Outline each uninfected red blood cell.
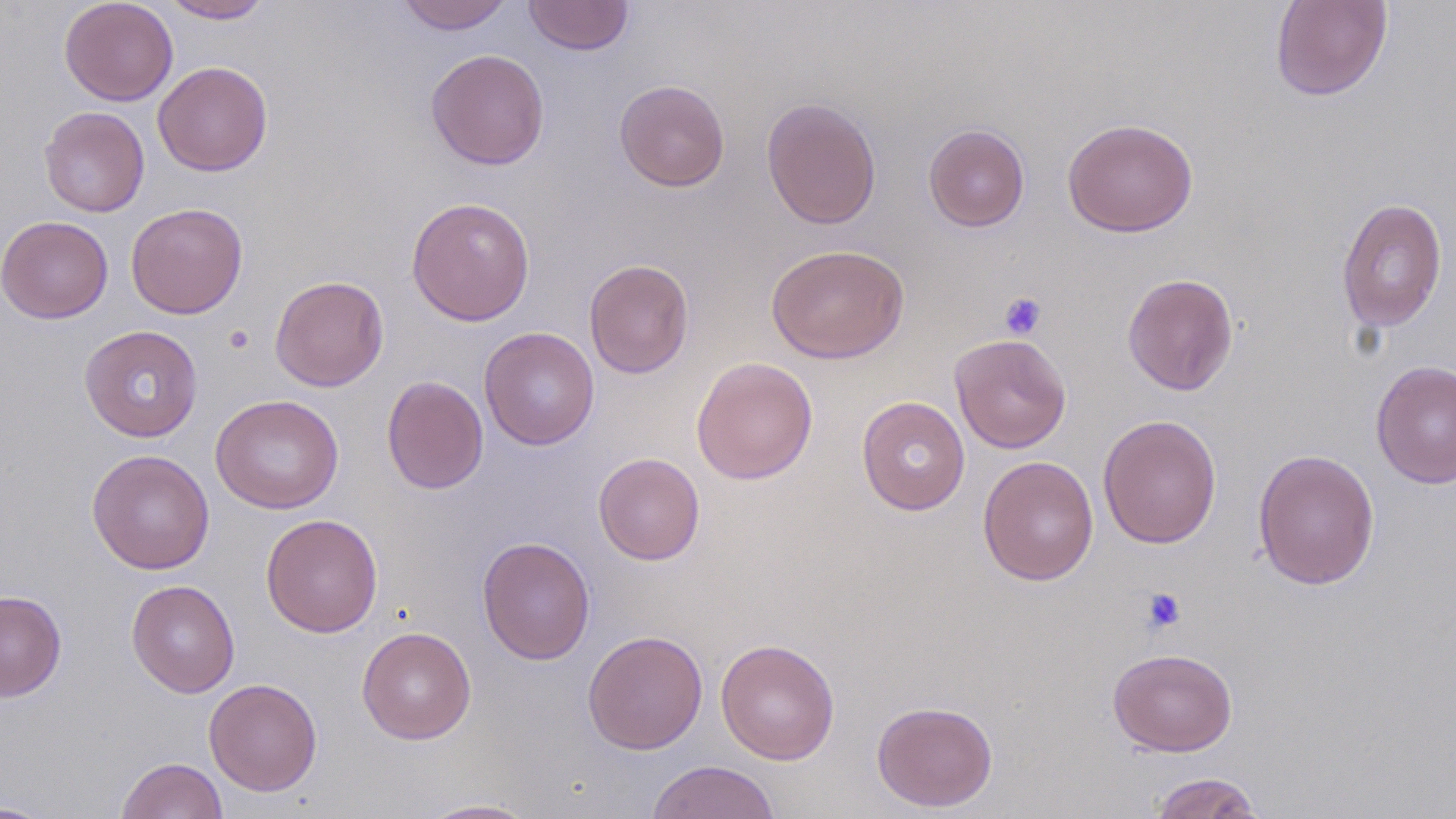
Approximate bounding boxes as (x1,y1)-(x2,y2) corner pairs in pixels.
Uninfected red blood cells: (59,0)-(178,106), (161,0)-(274,23), (396,0)-(514,34), (523,0)-(634,56), (1269,0)-(1393,101), (425,49)-(550,170), (153,61)-(273,176), (614,79)-(730,191), (761,97)-(882,229), (38,106)-(150,217), (1062,118)-(1198,237), (924,124)-(1030,232), (406,197)-(536,326), (1336,197)-(1448,334), (125,202)-(248,319), (0,216)-(114,324), (765,244)-(910,364), (584,259)-(694,379), (1122,273)-(1239,396), (269,275)-(389,392), (78,325)-(203,442), (479,327)-(599,450), (949,333)-(1072,453), (691,357)-(818,484), (1370,360)-(1456,489), (382,375)-(489,494), (210,394)-(344,514), (856,396)-(971,515), (1098,414)-(1222,549), (1252,448)-(1380,591), (87,449)-(215,574), (593,452)-(705,565), (977,455)-(1099,586), (260,513)-(383,637), (477,537)-(595,665), (126,579)-(240,697), (0,590)-(67,702), (356,626)-(476,744), (582,630)-(708,754), (715,638)-(840,765), (1107,647)-(1238,756), (203,678)-(322,796), (871,700)-(998,811), (116,757)-(228,818), (645,760)-(781,819), (1148,771)-(1266,818), (416,799)-(542,818), (0,800)-(57,818).

Summary:
  - Platelet locations: (999,292)-(1046,340), (224,325)-(254,354), (1140,586)-(1187,634)
  - Slide-level diagnosis: negative for blood parasites
  - Field of view: one of a larger specimen
  - Preparation: thin blood smear
  - Image size: 1456×819 pixels
  - Modality: optical microscopy
  - Stain: May-Grünwald-Giemsa
  - Magnification: 1000x